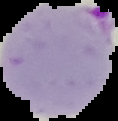

Result: Plasmodium parasites identified. The area outside the segmented cell region is set to black. From a thin blood film. Image is 118×121 pixels.